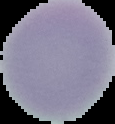

Summary:
  - Image size: 115×124 pixels
  - Preparation: thin blood film
  - Result: negative for malaria parasites
  - Image type: segmented cell region with the area outside set to black